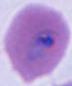
Micrograph. A Plasmodium parasite is shown. Captured at either 400x or 1000x magnification.